Report the malaria status of this cell.
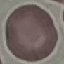
Uninfected.

Summary:
  - Stain: Giemsa
  - Capture: smartphone through the microscope eyepiece
  - Image type: cell patch, automatically extracted from a larger field of view and resized to 64 × 64 pixels
  - Preparation: thin smear